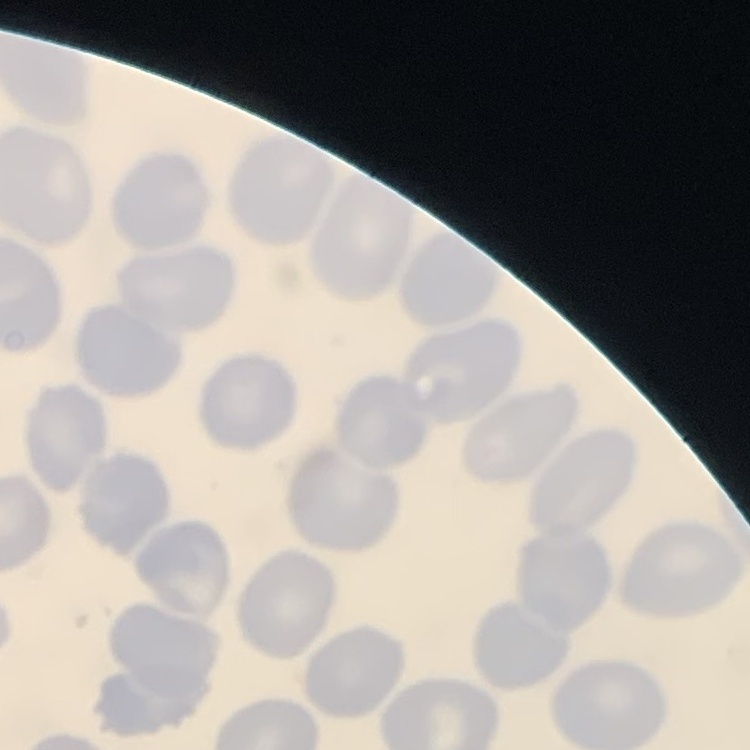
Summary:
  - Red blood cell morphology: no rouleaux formation
  - Stain: Field's or Giemsa
  - Image type: one tile cut from a larger photomicrograph
  - Preparation: thin blood film